Name the parasite shown.
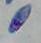

This is Toxoplasma gondii.

modality = photomicrograph
magnification = 1000x